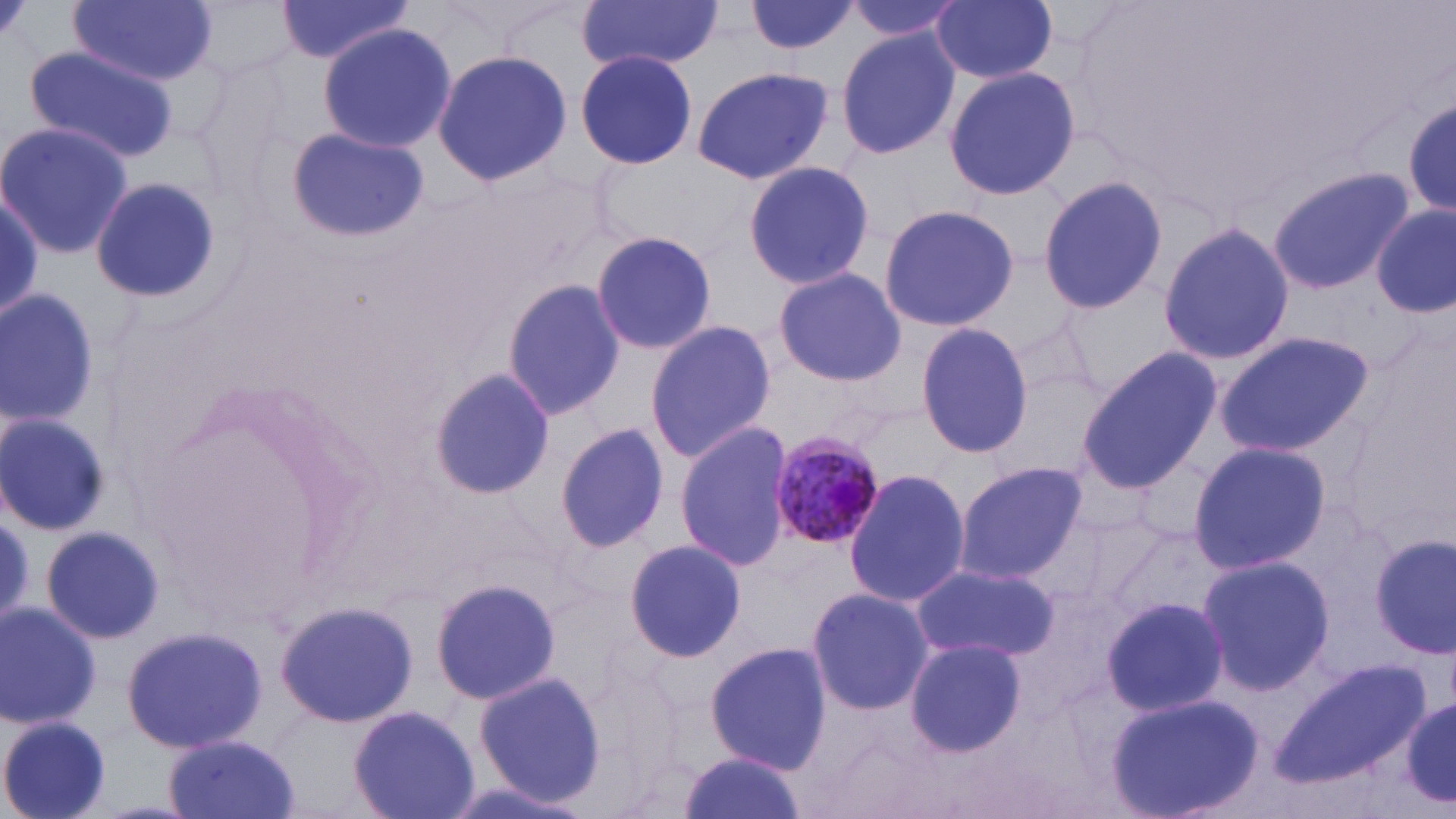

{
  "slide_level_diagnosis": "Plasmodium malariae",
  "field_of_view": "single",
  "preparation": "thin blood film",
  "modality": "light microscopy",
  "uninfected_red_blood_cell_locations": "approximate bounding boxes as (x1,y1)-(x2,y2) corner pairs in pixels: (68,0)-(218,85), (186,0)-(303,79), (575,0)-(728,74), (744,0)-(861,57), (841,0)-(964,45), (930,0)-(1059,85), (274,1)-(416,63), (317,23)-(455,154), (834,28)-(961,161), (23,45)-(177,162), (432,50)-(573,184), (575,50)-(698,169), (690,65)-(835,184), (942,67)-(1081,202), (1401,95)-(1456,223), (0,122)-(134,257), (286,126)-(428,243), (742,159)-(876,290), (1265,166)-(1414,295), (90,175)-(222,301), (1038,175)-(1170,316), (0,193)-(45,324), (879,203)-(1020,332), (1372,206)-(1454,316), (1157,222)-(1295,365), (590,229)-(718,357), (773,268)-(908,387), (500,277)-(625,422), (0,287)-(101,428), (1005,312)-(1102,408), (644,319)-(776,466), (915,322)-(1032,462), (1214,331)-(1374,459), (1077,347)-(1220,494), (427,366)-(554,502), (0,413)-(111,536), (674,421)-(796,572), (555,422)-(667,554), (1186,440)-(1330,577), (953,460)-(1088,585), (844,467)-(972,609), (0,512)-(37,623), (41,524)-(164,645), (1368,534)-(1454,659), (623,537)-(745,661), (1197,554)-(1336,691), (913,563)-(1059,662), (428,577)-(562,704), (804,587)-(933,715), (1101,596)-(1229,717), (0,601)-(101,729), (276,601)-(418,725), (122,626)-(267,753), (904,637)-(1029,757), (703,640)-(833,774), (1269,661)-(1430,787), (475,671)-(605,803), (1402,692)-(1456,812), (1106,693)-(1265,819), (349,703)-(480,818), (0,714)-(113,819), (162,732)-(298,819), (676,752)-(811,819)",
  "magnification": "1000x",
  "plasmodium_malariae_infected_red_blood_cell_locations": "approximate bounding boxes as (x1,y1)-(x2,y2) corner pairs in pixels: (765,433)-(884,553)",
  "stain": "May-Grünwald-Giemsa",
  "image_size": "1456×819 pixels"
}